Assess this cell for malaria.
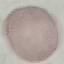

Uninfected.

stain: Giemsa
capture: smartphone through the microscope eyepiece
preparation: thin blood smear
image_type: automatically extracted cell patch, resized to 64 × 64 pixels